Report the malaria status of this cell.
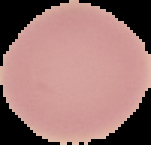
Uninfected.

image size = 151×145 pixels
preparation = thin blood smear
image type = cell region segmented out of the field of view; surrounding area masked to black